Locate and identify every blood parasite.
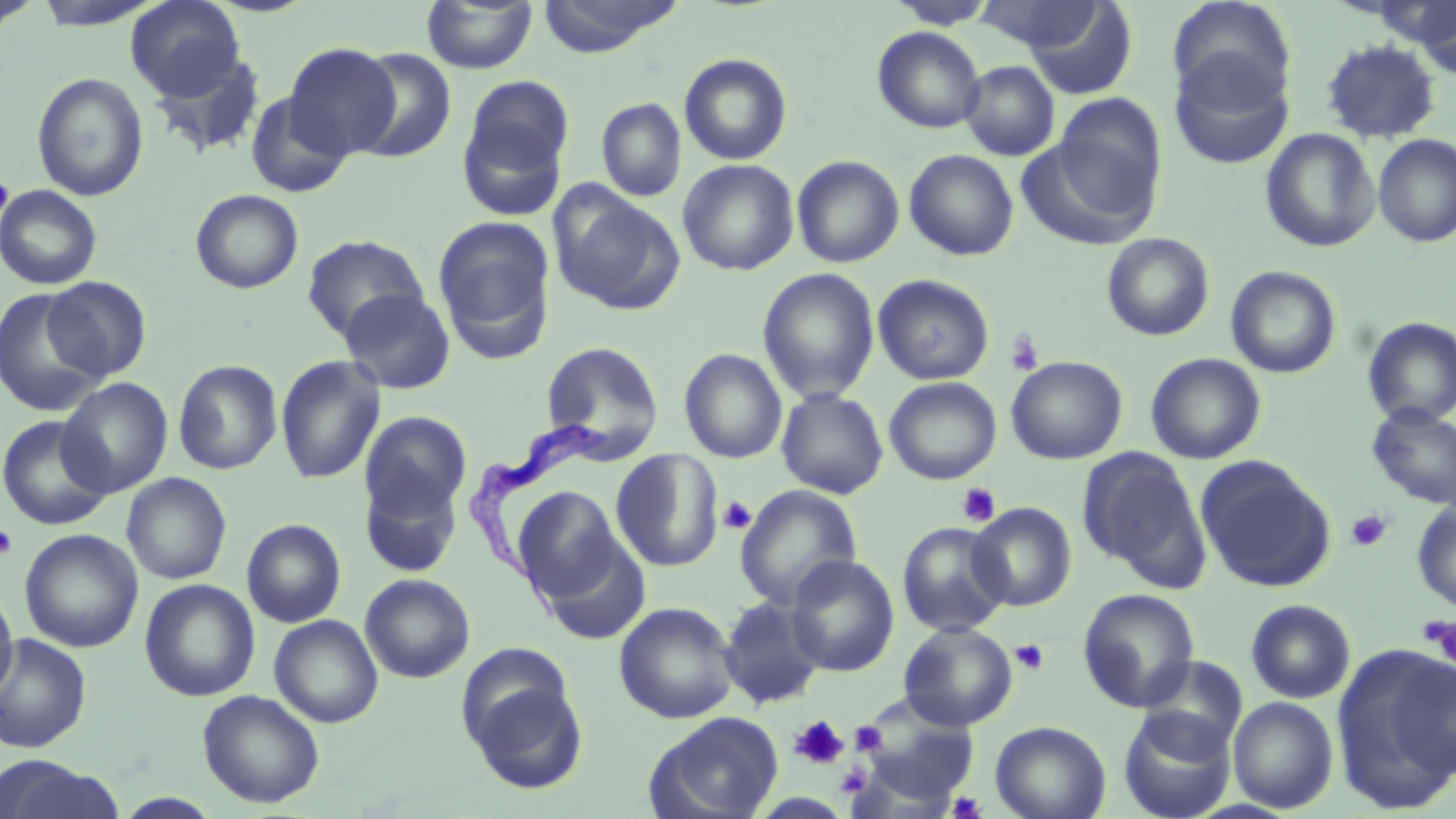
Approximate bounding boxes as named x1/y1/x2/y2 corners in pixels.
Trypanosoma brucei: (x1=460, y1=420, x2=614, y2=618).
No Plasmodium falciparum, Plasmodium ovale, Plasmodium malariae, Plasmodium vivax, or Babesia divergens observed.

Uninfected red blood cell locations: (x1=0, y1=0, x2=41, y2=36), (x1=126, y1=0, x2=246, y2=100), (x1=421, y1=0, x2=538, y2=75), (x1=536, y1=0, x2=686, y2=56), (x1=887, y1=0, x2=999, y2=29), (x1=974, y1=0, x2=1104, y2=55), (x1=29, y1=1, x2=164, y2=29), (x1=1023, y1=1, x2=1137, y2=100), (x1=1167, y1=1, x2=1297, y2=110), (x1=1411, y1=2, x2=1456, y2=79), (x1=871, y1=26, x2=985, y2=132), (x1=1320, y1=39, x2=1442, y2=144), (x1=285, y1=43, x2=400, y2=158), (x1=147, y1=48, x2=268, y2=160), (x1=350, y1=48, x2=457, y2=163), (x1=679, y1=52, x2=793, y2=165), (x1=1169, y1=53, x2=1293, y2=170), (x1=959, y1=60, x2=1059, y2=160), (x1=31, y1=72, x2=149, y2=201), (x1=458, y1=79, x2=574, y2=218), (x1=244, y1=91, x2=354, y2=198), (x1=1051, y1=92, x2=1167, y2=225), (x1=596, y1=97, x2=686, y2=202), (x1=1260, y1=128, x2=1380, y2=252), (x1=1373, y1=134, x2=1456, y2=247), (x1=904, y1=149, x2=1019, y2=261), (x1=792, y1=155, x2=904, y2=268), (x1=678, y1=159, x2=799, y2=276), (x1=549, y1=183, x2=684, y2=316), (x1=0, y1=185, x2=103, y2=290), (x1=190, y1=189, x2=304, y2=294), (x1=433, y1=215, x2=556, y2=360), (x1=1101, y1=233, x2=1215, y2=341), (x1=301, y1=234, x2=429, y2=342), (x1=1225, y1=265, x2=1342, y2=378), (x1=757, y1=267, x2=880, y2=403), (x1=872, y1=273, x2=995, y2=385), (x1=43, y1=276, x2=152, y2=381), (x1=0, y1=288, x2=109, y2=416), (x1=339, y1=288, x2=455, y2=395), (x1=1362, y1=317, x2=1456, y2=428), (x1=540, y1=341, x2=664, y2=458), (x1=679, y1=348, x2=787, y2=463), (x1=1145, y1=353, x2=1266, y2=464), (x1=275, y1=355, x2=386, y2=484), (x1=1006, y1=356, x2=1127, y2=464), (x1=173, y1=360, x2=283, y2=475), (x1=58, y1=377, x2=173, y2=498), (x1=884, y1=377, x2=1002, y2=485), (x1=777, y1=388, x2=888, y2=499), (x1=1366, y1=404, x2=1456, y2=510), (x1=360, y1=411, x2=472, y2=524), (x1=0, y1=414, x2=114, y2=531), (x1=611, y1=449, x2=724, y2=571), (x1=1077, y1=449, x2=1206, y2=582), (x1=1195, y1=456, x2=1336, y2=592), (x1=359, y1=466, x2=464, y2=578), (x1=129, y1=471, x2=245, y2=691), (x1=121, y1=472, x2=232, y2=584), (x1=735, y1=484, x2=862, y2=610), (x1=513, y1=486, x2=623, y2=600), (x1=1412, y1=500, x2=1456, y2=612), (x1=969, y1=502, x2=1076, y2=612), (x1=242, y1=519, x2=346, y2=627), (x1=897, y1=522, x2=1011, y2=636), (x1=19, y1=529, x2=143, y2=652), (x1=539, y1=538, x2=651, y2=644), (x1=786, y1=555, x2=899, y2=677), (x1=359, y1=573, x2=475, y2=683), (x1=139, y1=578, x2=260, y2=701), (x1=0, y1=585, x2=18, y2=703), (x1=1077, y1=588, x2=1200, y2=712), (x1=718, y1=595, x2=828, y2=709), (x1=1246, y1=600, x2=1356, y2=703), (x1=614, y1=602, x2=739, y2=723), (x1=269, y1=615, x2=383, y2=728), (x1=898, y1=622, x2=1018, y2=730), (x1=0, y1=634, x2=92, y2=753), (x1=1333, y1=650, x2=1456, y2=810), (x1=1388, y1=653, x2=1456, y2=780), (x1=1134, y1=657, x2=1247, y2=757), (x1=461, y1=665, x2=589, y2=796), (x1=197, y1=689, x2=325, y2=808), (x1=1228, y1=697, x2=1339, y2=813), (x1=1118, y1=708, x2=1237, y2=819), (x1=647, y1=713, x2=784, y2=819), (x1=990, y1=721, x2=1111, y2=819), (x1=0, y1=757, x2=124, y2=819), (x1=115, y1=792, x2=224, y2=818). Platelet locations: (x1=0, y1=170, x2=14, y2=233), (x1=1005, y1=330, x2=1045, y2=377), (x1=957, y1=482, x2=1001, y2=527), (x1=717, y1=495, x2=757, y2=535), (x1=1346, y1=509, x2=1392, y2=552), (x1=0, y1=522, x2=18, y2=559), (x1=1420, y1=614, x2=1456, y2=664), (x1=1010, y1=639, x2=1050, y2=676), (x1=789, y1=714, x2=849, y2=770), (x1=850, y1=720, x2=887, y2=756), (x1=836, y1=764, x2=871, y2=798), (x1=947, y1=790, x2=987, y2=818). Slide-level diagnosis: Trypanosoma brucei. Captured at 1000x magnification. Optical microscopy. Image is 1456×819 pixels. Thin blood film. May-Grünwald-Giemsa-stained preparation. One field of a larger specimen.